Assess this cell for malaria.
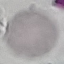
It is uninfected.

Summary:
  - Preparation: thin blood smear
  - Image type: cell patch, automatically extracted from a larger field of view and resized to 64 × 64 pixels
  - Capture: smartphone camera at the microscope eyepiece
  - Stain: Giemsa